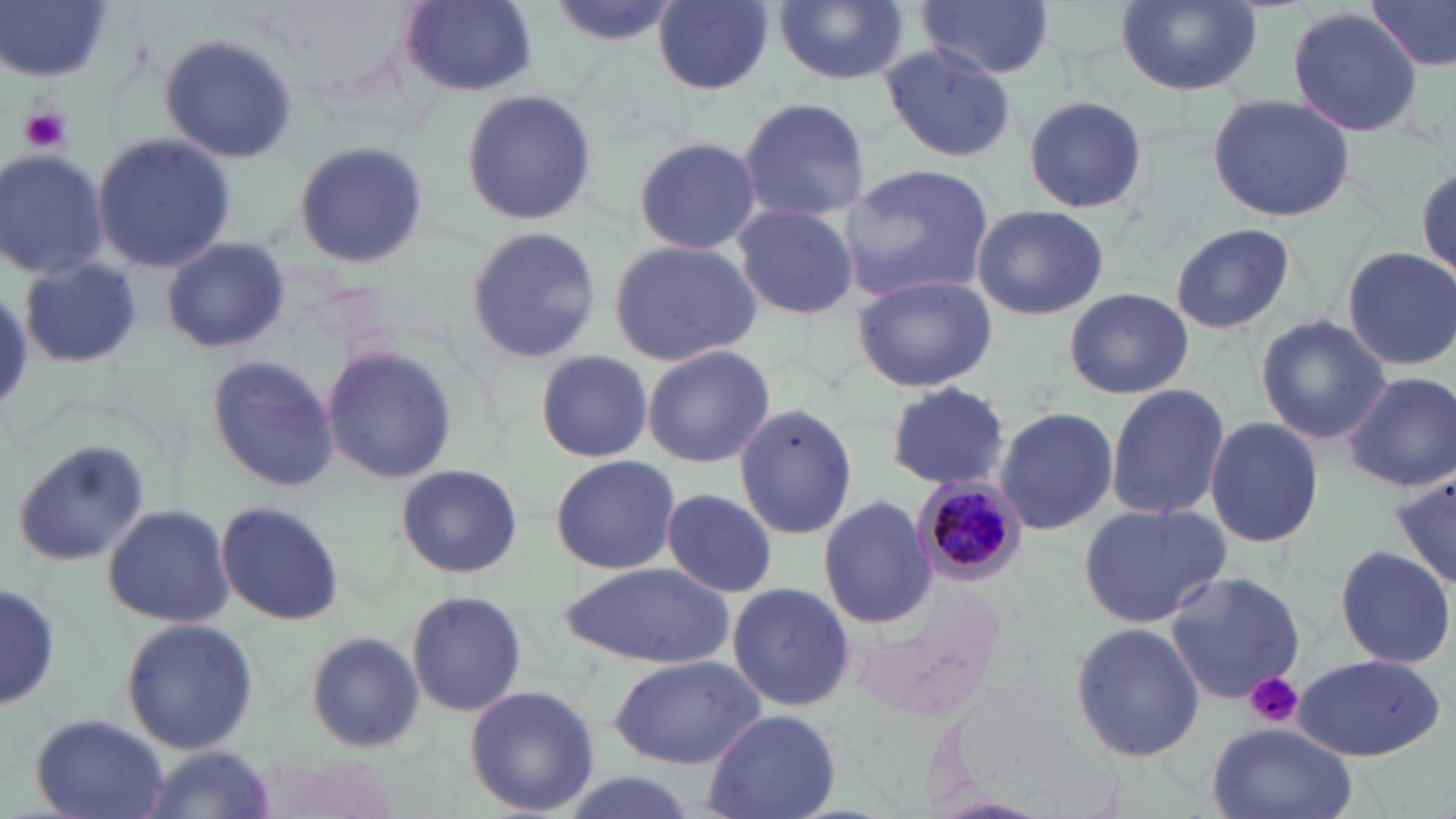 Approximate bounding boxes as (x1, y1, x2, y2) in pixels. Platelet locations: (21, 107, 71, 153), (1244, 672, 1304, 727). Uninfected red blood cell locations: (397, 0, 538, 97), (548, 0, 678, 49), (655, 0, 775, 94), (773, 0, 912, 86), (918, 0, 1055, 77), (1368, 0, 1456, 72), (2, 2, 116, 83), (1117, 2, 1262, 95), (1286, 7, 1426, 137), (160, 32, 302, 166), (879, 42, 1017, 164), (460, 89, 597, 226), (1208, 93, 1356, 223), (736, 95, 871, 220), (1021, 96, 1149, 214), (91, 133, 236, 271), (631, 136, 765, 255), (293, 138, 429, 270), (1, 148, 110, 281), (1409, 161, 1456, 275), (838, 162, 995, 302), (731, 202, 858, 319), (972, 206, 1108, 320), (1170, 222, 1295, 335), (464, 226, 602, 364), (159, 235, 290, 354), (607, 238, 762, 367), (1342, 247, 1454, 369), (19, 257, 141, 368), (851, 273, 995, 391), (1065, 287, 1194, 400), (1256, 315, 1390, 444), (642, 345, 774, 467), (320, 347, 457, 484), (535, 349, 652, 462), (205, 355, 336, 489), (1343, 370, 1455, 492), (886, 380, 1012, 493), (1105, 383, 1229, 521), (733, 404, 858, 540), (994, 405, 1120, 537), (1206, 416, 1322, 548), (8, 440, 152, 569), (549, 455, 679, 575), (397, 465, 521, 578), (1390, 470, 1455, 592), (661, 488, 777, 598), (818, 495, 936, 629), (216, 501, 344, 625), (102, 502, 234, 629), (1077, 502, 1232, 629), (1333, 543, 1454, 669), (560, 564, 733, 666), (1164, 570, 1306, 704), (2, 579, 59, 715), (725, 582, 855, 714), (405, 590, 527, 719), (119, 617, 260, 757), (1069, 622, 1206, 763), (304, 632, 426, 755), (608, 655, 767, 770), (1294, 655, 1446, 761), (464, 683, 600, 817), (701, 709, 841, 819), (29, 713, 171, 819), (1206, 721, 1357, 819), (135, 747, 277, 819), (557, 770, 702, 819). Plasmodium malariae-infected red blood cell locations: (913, 474, 1028, 587). Slide-level diagnosis: Plasmodium malariae. 1000x magnification. Image is 1456×819 pixels. Thin blood smear. Optical microscopy. Single field of view. May-Grünwald-Giemsa-stained preparation.